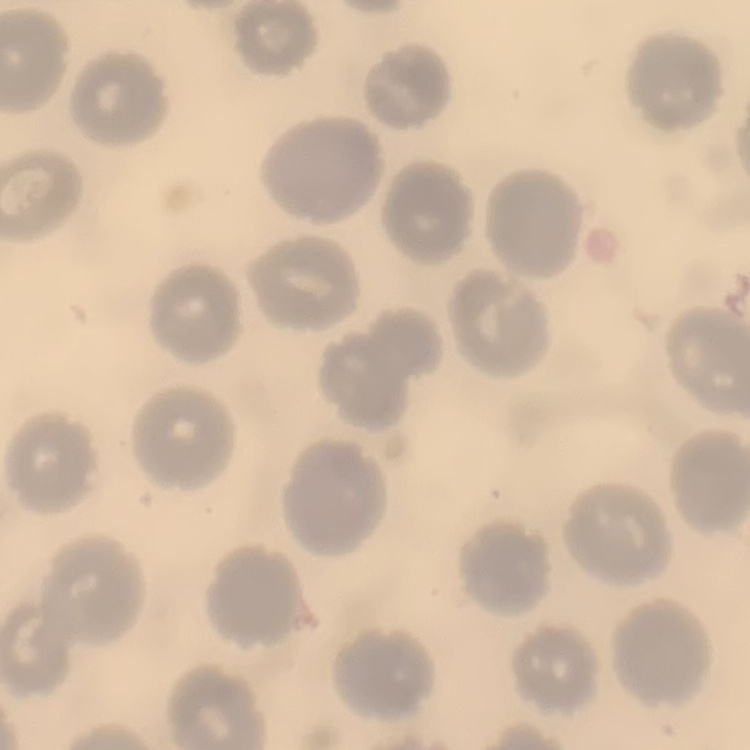
Summary:
  - Erythrocyte morphology: no rouleaux formation
  - Stain: Field's or Giemsa
  - Preparation: thin blood smear
  - Image type: one tile cut from a larger photomicrograph